State the blood parasite species.
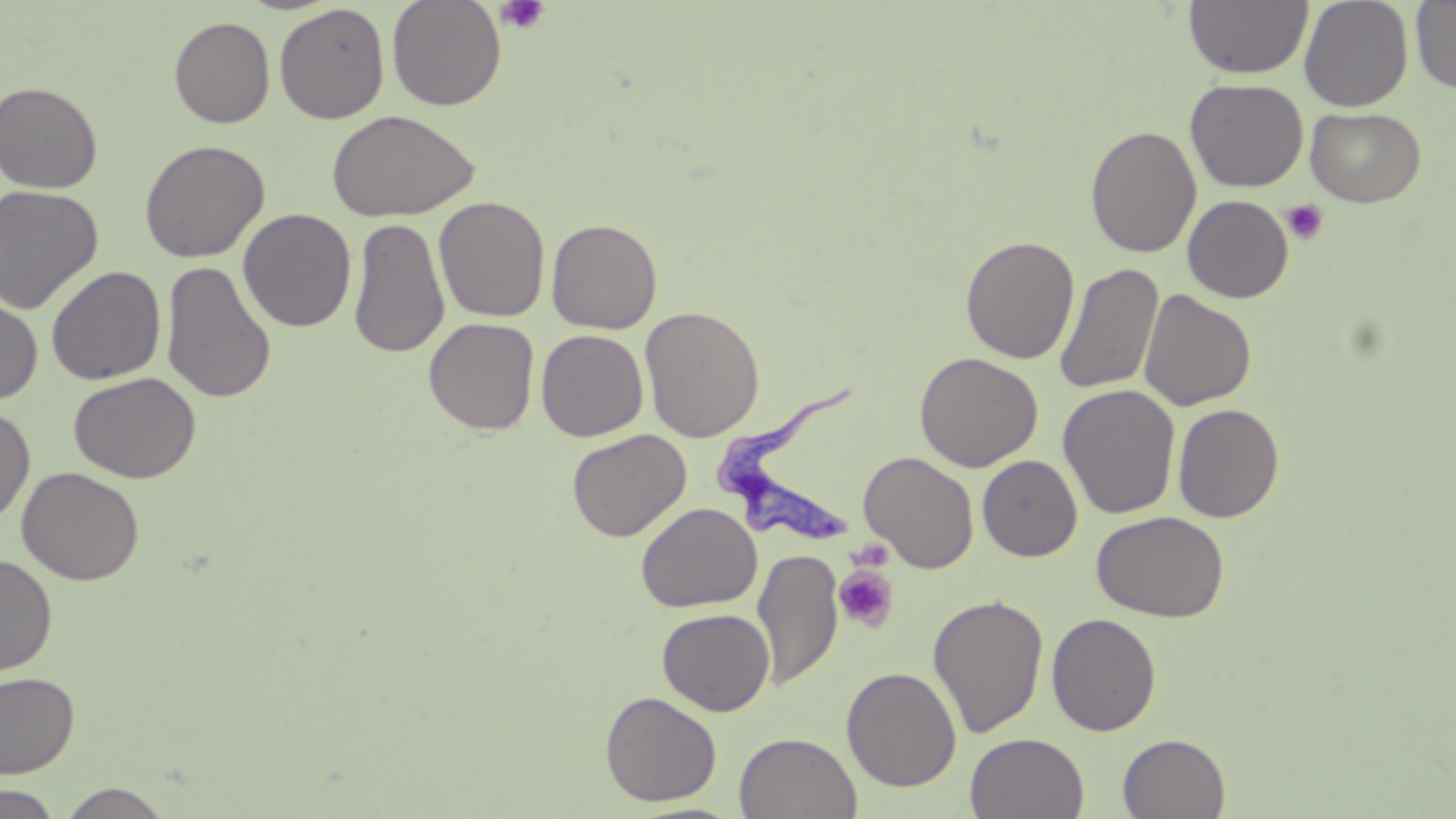

Trypanosoma brucei.

Approximate bounding boxes as [x1, y1, x2, y2] in pixels. Uninfected red blood cell locations: [386, 0, 507, 111], [1183, 0, 1313, 79], [1299, 0, 1414, 112], [1411, 1, 1456, 93], [273, 3, 390, 124], [169, 16, 275, 128], [1185, 78, 1308, 192], [0, 81, 103, 193], [1305, 107, 1426, 207], [326, 109, 480, 223], [1085, 124, 1202, 258], [139, 139, 270, 263], [0, 185, 104, 314], [1182, 195, 1294, 303], [434, 196, 550, 322], [237, 208, 357, 332], [347, 215, 450, 359], [546, 218, 663, 334], [960, 234, 1080, 364], [161, 259, 277, 405], [1054, 263, 1163, 395], [46, 264, 166, 385], [0, 289, 43, 406], [1139, 289, 1256, 412], [639, 305, 765, 442], [423, 317, 540, 435], [536, 329, 649, 441], [915, 352, 1043, 472], [69, 371, 201, 484], [1058, 384, 1181, 520], [1172, 403, 1285, 523], [0, 405, 36, 524], [567, 428, 692, 542], [859, 451, 979, 573], [978, 455, 1083, 562], [17, 466, 144, 586], [636, 502, 762, 612], [1091, 510, 1230, 623], [752, 549, 843, 691], [0, 554, 58, 676], [927, 594, 1049, 739], [657, 608, 775, 715], [1047, 613, 1162, 736], [841, 666, 962, 792], [0, 671, 80, 779], [600, 691, 722, 807], [733, 732, 863, 819], [965, 733, 1089, 818], [1117, 733, 1231, 818], [58, 783, 173, 818], [0, 784, 63, 819], [624, 800, 749, 819]. Platelet locations: [495, 0, 550, 35], [1282, 200, 1329, 245], [846, 539, 895, 572], [833, 564, 899, 632]. Trypanosoma brucei locations: [714, 373, 860, 540]. Image is 1456×819 pixels. Thin blood smear. May-Grünwald-Giemsa stain. One field of a larger specimen. 1000x magnification. Light microscopy.